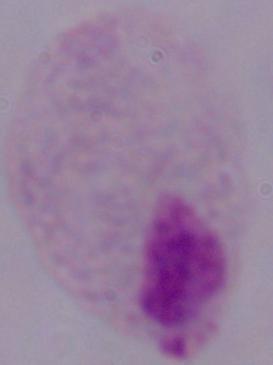

Summary:
  - Modality: photomicrograph
  - Identification: trichomonad
  - Magnification: 1000x